Comment on the morphology of the red blood cells.
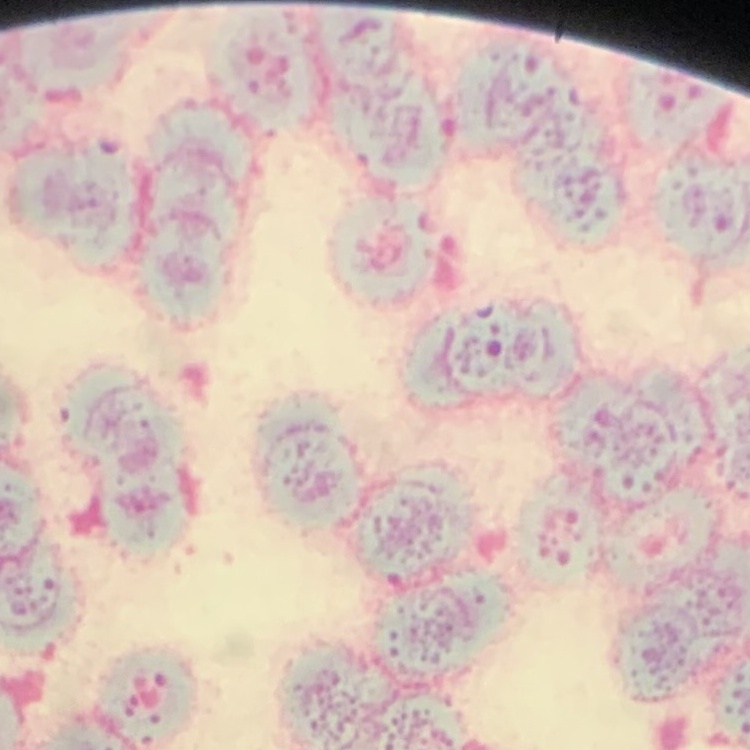

Rouleaux formation.

Summary:
  - Stain: Field's or Giemsa
  - Image type: square crop of a larger photomicrograph
  - Preparation: thin blood film